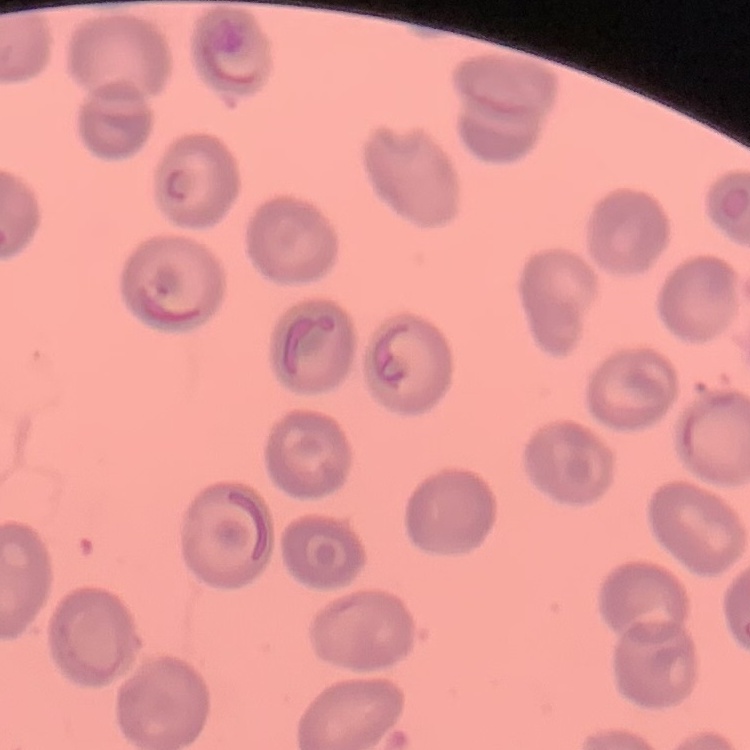

The red blood cells exhibit no rouleaux formation. Stained with either Field's or Giemsa. Thin blood smear. One tile cut from a larger photomicrograph.